Look for Plasmodium parasites.
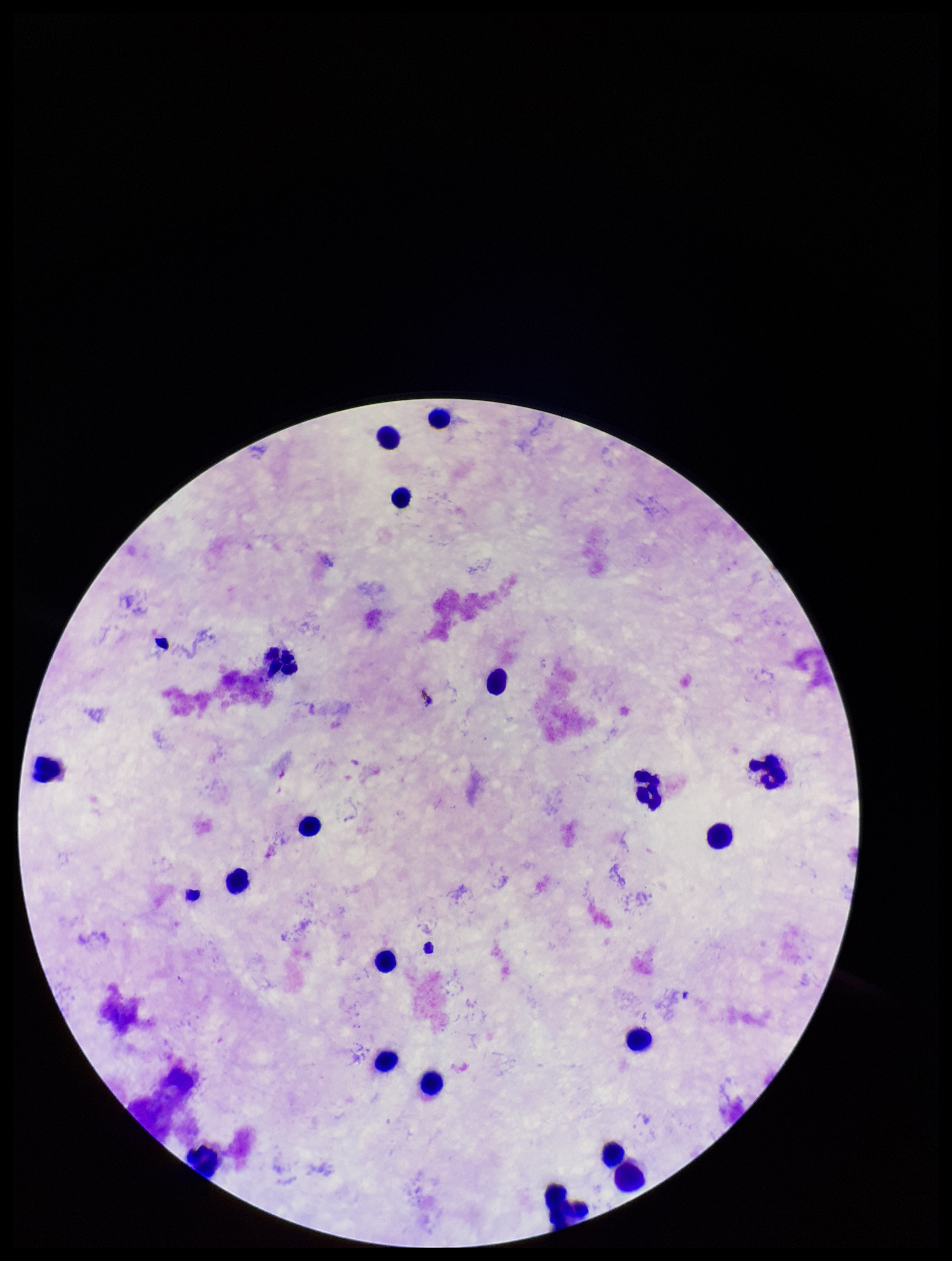
None detected.

stain = Giemsa
preparation = thick smear
image size = 952×1261 pixels
patient malaria status = negative
parasite count = 0
field of view = single
leukocyte count = 20
capture = smartphone photograph through the microscope eyepiece